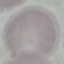

malaria status = uninfected
image type = cell patch, automatically extracted from a larger field of view and resized to 64 × 64 pixels
stain = Giemsa
preparation = thin smear
capture = smartphone through the microscope eyepiece